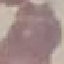
result = no malaria parasites seen
preparation = thin blood film
stain = Giemsa
image type = automatically extracted cell patch, resized to 64 × 64 pixels
capture = smartphone through the microscope eyepiece